Identify the parasite.
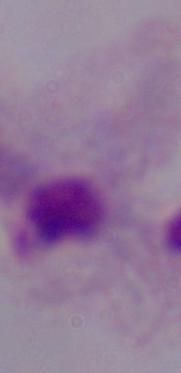

This is a trichomonad.

1000x magnification. Photomicrograph.